Classify this cell by malaria status.
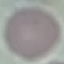
Uninfected.

Summary:
  - Stain: Giemsa
  - Image type: automatically extracted cell patch, resized to 64 × 64 pixels
  - Capture: smartphone camera at the microscope eyepiece
  - Preparation: thin smear